Locate every blood parasite and identify its species.
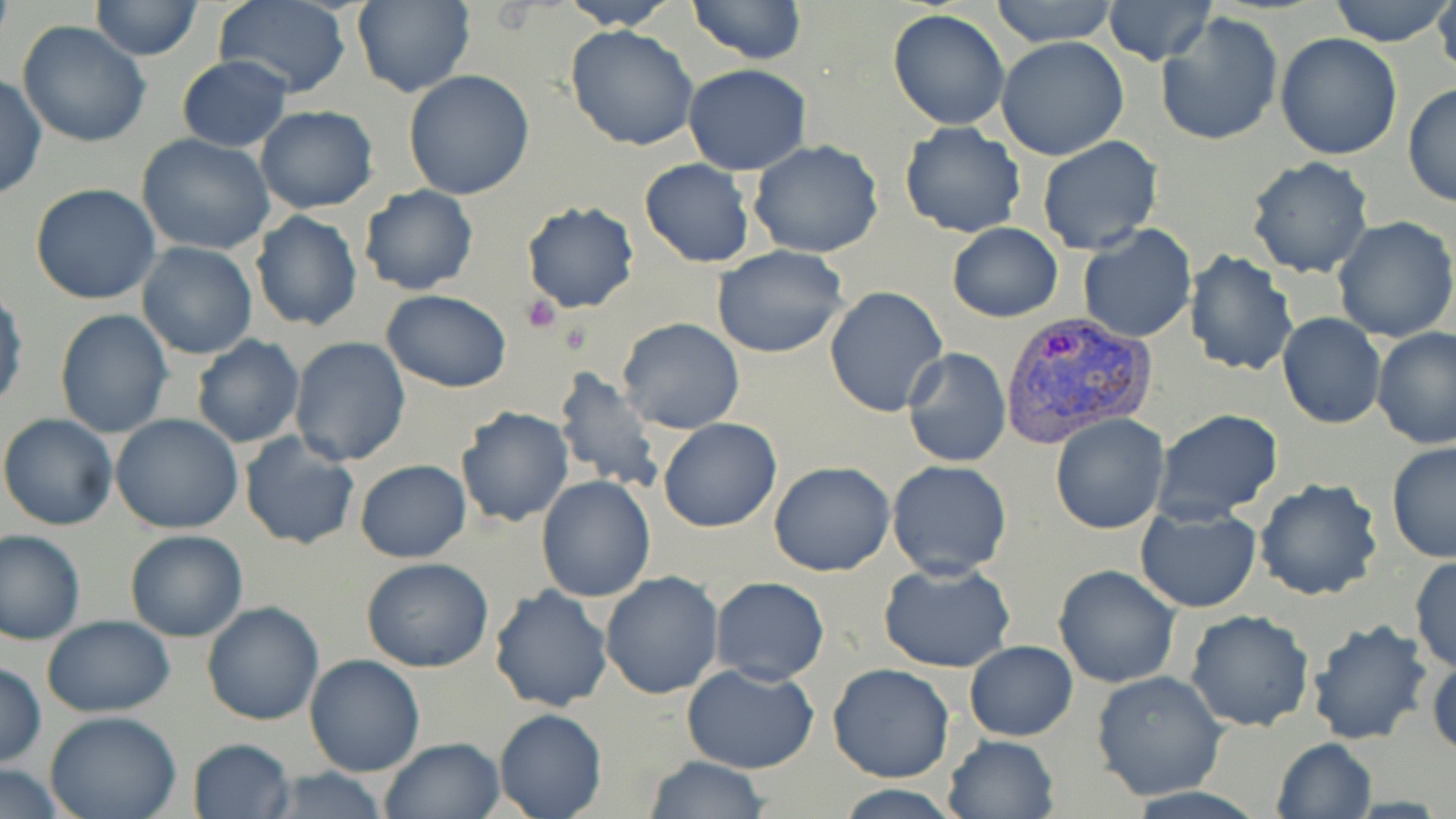

Approximate bounding boxes as [x1, y1, x2, y2] in pixels.
Plasmodium vivax-infected red blood cells: [999, 314, 1157, 444].
No Plasmodium falciparum, Plasmodium ovale, Plasmodium malariae, Babesia divergens, or Trypanosoma brucei observed.

Uninfected red blood cell locations: [91, 0, 203, 60], [212, 0, 353, 98], [351, 0, 474, 98], [558, 0, 678, 30], [685, 0, 804, 65], [991, 0, 1117, 47], [1329, 0, 1454, 47], [1432, 0, 1456, 79], [1104, 1, 1216, 66], [887, 9, 1011, 129], [1155, 13, 1283, 147], [16, 21, 152, 148], [566, 24, 699, 151], [1276, 32, 1403, 158], [996, 37, 1129, 159], [177, 55, 293, 152], [682, 63, 811, 175], [403, 69, 535, 198], [0, 74, 47, 199], [1403, 84, 1455, 207], [255, 105, 379, 214], [899, 123, 1026, 240], [137, 133, 276, 256], [1036, 136, 1163, 256], [748, 140, 884, 258], [1245, 157, 1375, 279], [639, 158, 756, 269], [29, 183, 161, 306], [358, 185, 480, 295], [520, 201, 639, 314], [249, 211, 363, 331], [1332, 215, 1456, 341], [946, 222, 1064, 322], [1077, 224, 1198, 345], [139, 226, 363, 344], [136, 241, 257, 359], [713, 245, 849, 358], [1185, 250, 1299, 378], [0, 284, 26, 415], [824, 287, 948, 417], [383, 291, 512, 393], [53, 309, 173, 438], [1277, 312, 1386, 430], [617, 318, 745, 434], [1372, 326, 1456, 448], [191, 336, 305, 450], [289, 337, 412, 467], [903, 347, 1011, 467], [550, 367, 665, 496], [457, 408, 573, 528], [1153, 408, 1283, 522], [0, 412, 120, 530], [111, 414, 243, 534], [1049, 414, 1169, 534], [658, 418, 782, 532], [239, 432, 360, 551], [1384, 441, 1455, 564], [354, 459, 470, 562], [886, 459, 1012, 579], [769, 461, 895, 577], [536, 476, 656, 603], [1254, 478, 1385, 603], [1135, 504, 1261, 612], [1, 528, 85, 645], [124, 530, 249, 642], [1409, 555, 1456, 672], [361, 557, 494, 673], [877, 560, 1019, 675], [1052, 564, 1181, 688], [600, 572, 725, 699], [710, 575, 830, 686], [489, 585, 613, 714], [202, 601, 326, 725], [1184, 609, 1315, 732], [41, 615, 176, 716], [1305, 619, 1433, 747], [965, 641, 1077, 741], [1427, 650, 1456, 761], [303, 655, 426, 777], [0, 663, 46, 767], [829, 663, 956, 783], [682, 664, 820, 774], [1090, 671, 1227, 801], [494, 709, 606, 819], [44, 711, 184, 819], [943, 734, 1058, 819], [379, 736, 506, 819], [188, 737, 295, 818], [1271, 737, 1378, 819], [644, 755, 768, 819], [0, 766, 71, 817], [258, 766, 393, 819], [830, 785, 969, 818]. Platelet locations: [521, 295, 562, 333]. Slide-level diagnosis: Plasmodium vivax. Thin blood smear. Captured at 1000x magnification. May-Grünwald-Giemsa-stained preparation. One field of a larger specimen. Light microscopy. Image is 1456×819 pixels.